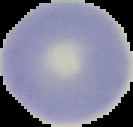

{
  "image_size": "133×127 pixels",
  "preparation": "thin blood smear",
  "malaria_status": "uninfected",
  "image_type": "cell region segmented out of the field of view; surrounding area masked to black"
}